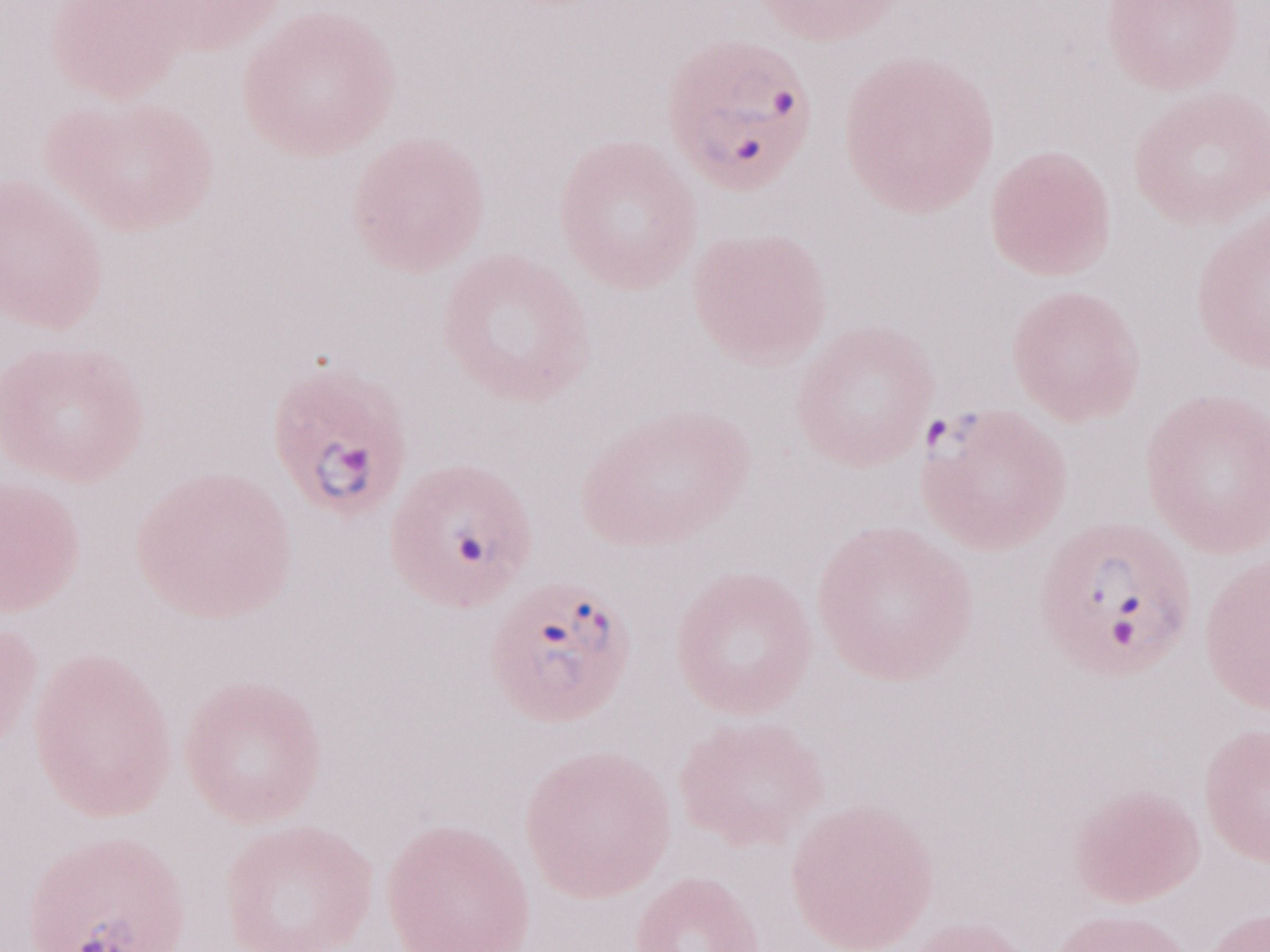
May-Grünwald-Giemsa (MGG) stain. Thin peripheral-blood smear. One field of this slide. Olympus BX43 microscope and DP73 digital camera. Image is 1270×952 pixels. 1,000x magnification. Malaria diagnosis (patient-level): positive.